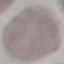
result = no malaria parasites seen
image type = cell patch, automatically extracted from a larger field of view and resized to 64 × 64 pixels
preparation = thin blood smear
capture = smartphone through the microscope eyepiece
stain = Giemsa